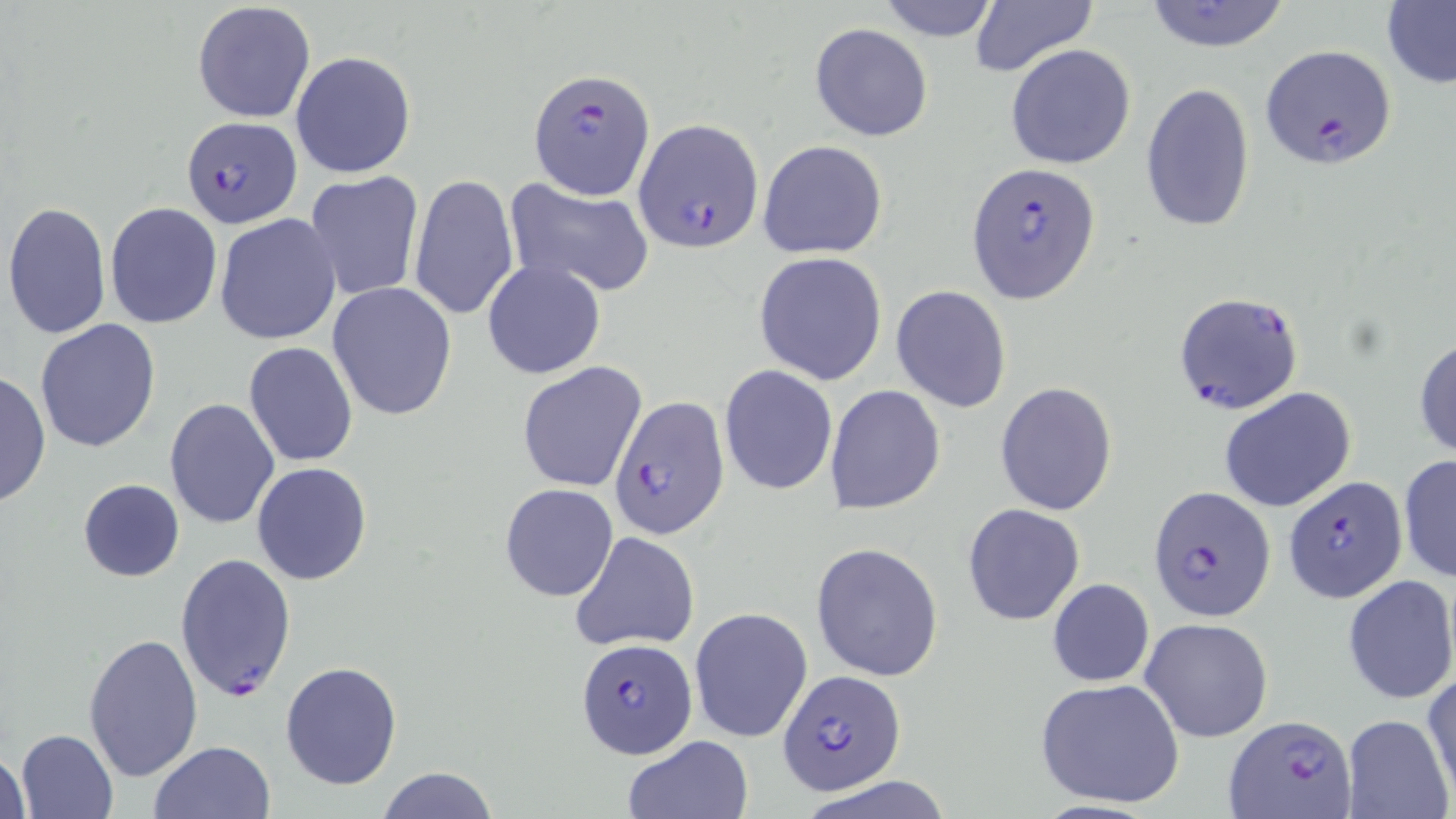

Summary:
  - Coordinate format: approximate bounding boxes as (x1,y1)-(x2,y2) corner pairs in pixels
  - Plasmodium falciparum-infected red blood cell locations: (1261,46)-(1396,170), (528,67)-(654,200), (180,116)-(301,229), (634,119)-(764,254), (966,163)-(1101,305), (1172,290)-(1304,415), (608,395)-(730,539), (1283,473)-(1409,605), (1148,485)-(1276,621), (174,552)-(297,701), (575,638)-(699,756), (780,670)-(905,795), (1226,713)-(1357,819)
  - Uninfected red blood cell locations: (876,0)-(1002,41), (967,0)-(1096,78), (1142,0)-(1295,53), (1381,0)-(1456,90), (192,2)-(316,124), (810,23)-(934,140), (1005,44)-(1136,170), (290,51)-(417,179), (1140,82)-(1256,234), (758,139)-(889,259), (303,172)-(424,302), (409,174)-(520,322), (503,176)-(656,298), (3,201)-(113,341), (105,201)-(222,328), (214,214)-(342,345), (754,253)-(887,386), (483,259)-(606,381), (327,282)-(458,420), (891,286)-(1012,414), (34,320)-(161,452), (1413,334)-(1456,462), (244,342)-(358,467), (517,362)-(646,493), (719,365)-(838,496), (0,370)-(50,508), (994,382)-(1119,515), (825,384)-(945,514), (1219,387)-(1356,513), (164,398)-(281,530), (1398,453)-(1456,587), (251,462)-(375,586), (77,479)-(184,583), (498,483)-(618,602), (962,503)-(1085,627), (570,530)-(700,652), (812,542)-(944,681), (1340,574)-(1456,705), (1046,578)-(1155,688), (690,607)-(813,742), (1140,617)-(1274,743), (81,631)-(202,782), (280,661)-(402,791), (1424,670)-(1456,803), (1034,677)-(1186,809), (1341,714)-(1452,819), (15,729)-(120,818), (621,736)-(753,819), (150,740)-(277,819), (1,747)-(30,819), (375,767)-(499,819), (797,776)-(958,818)
  - Slide-level diagnosis: Plasmodium falciparum
  - Field of view: one of a larger specimen
  - Preparation: thin blood film
  - Magnification: 1000x
  - Image size: 1456×819 pixels
  - Modality: light microscopy
  - Stain: May-Grünwald-Giemsa